Identify the parasite.
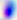
Toxoplasma gondii.

Photomicrograph. Captured at 400x magnification.